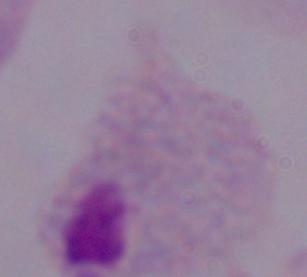

{
  "identification": "trichomonad",
  "magnification": "1000x",
  "modality": "micrograph"
}